Locate every Plasmodium ovale-infected red blood cell.
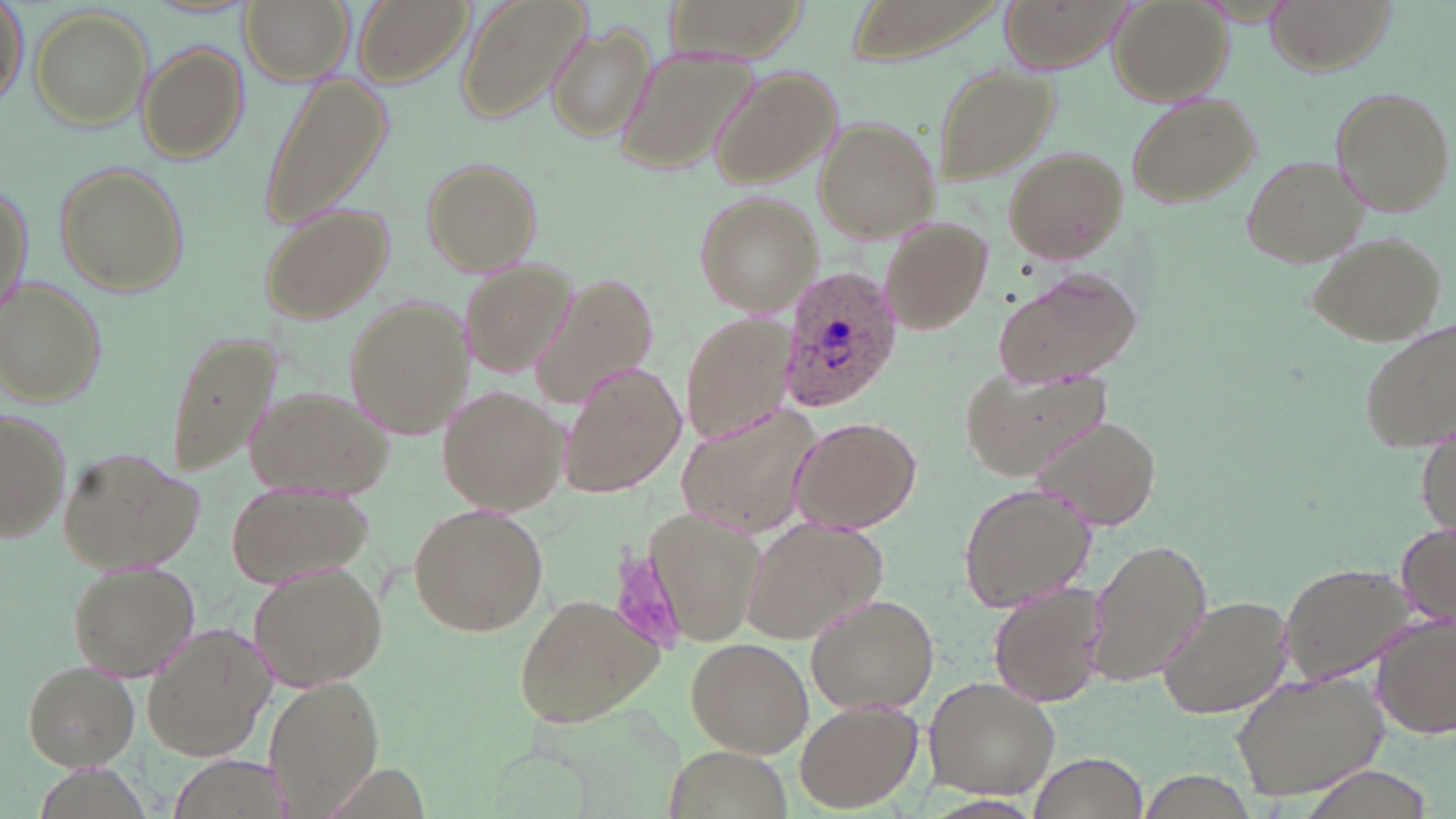

Approximate bounding boxes as [x1, y1, x2, y2] in pixels.
Plasmodium ovale-infected red blood cells: [779, 265, 902, 414].

Summary:
  - Uninfected red blood cell locations: [240, 0, 353, 84], [357, 0, 471, 84], [456, 0, 587, 119], [1001, 0, 1126, 69], [1108, 0, 1232, 106], [1263, 0, 1393, 72], [2, 1, 28, 108], [665, 3, 808, 69], [847, 3, 1000, 67], [30, 8, 153, 129], [548, 21, 655, 144], [137, 42, 247, 163], [615, 45, 757, 178], [928, 61, 1059, 185], [708, 66, 840, 191], [257, 72, 390, 228], [1328, 86, 1455, 217], [1124, 91, 1261, 209], [813, 114, 942, 244], [1003, 146, 1128, 262], [1240, 153, 1369, 266], [421, 157, 542, 278], [52, 162, 189, 300], [1, 175, 34, 315], [692, 190, 819, 316], [258, 204, 396, 326], [878, 216, 994, 335], [1308, 230, 1448, 344], [459, 258, 579, 377], [993, 266, 1143, 389], [534, 272, 660, 410], [0, 277, 108, 408], [343, 300, 474, 438], [682, 313, 793, 444], [1357, 320, 1454, 453], [163, 329, 282, 482], [560, 363, 684, 499], [959, 363, 1109, 484], [246, 384, 388, 493], [437, 387, 566, 515], [677, 398, 820, 537], [0, 406, 72, 548], [1032, 414, 1164, 534], [789, 415, 920, 532], [1416, 428, 1454, 541], [58, 445, 202, 575], [958, 480, 1094, 615], [227, 481, 373, 586], [408, 502, 549, 637], [644, 509, 769, 649], [741, 516, 886, 645], [1394, 522, 1456, 629], [1088, 538, 1212, 689], [68, 560, 199, 679], [249, 560, 388, 692], [1280, 561, 1414, 685], [987, 580, 1106, 705], [512, 592, 665, 730], [805, 593, 940, 716], [1157, 593, 1294, 718], [1372, 614, 1455, 740], [141, 625, 273, 760], [684, 636, 813, 757], [19, 659, 141, 769], [1231, 669, 1389, 801], [262, 674, 385, 814], [923, 677, 1063, 800], [793, 701, 920, 811], [657, 743, 794, 819], [1027, 750, 1151, 819]
  - Slide-level diagnosis: Plasmodium ovale
  - Modality: optical microscopy
  - Stain: May-Grünwald-Giemsa
  - Field of view: single
  - Magnification: 1000x
  - Preparation: thin blood smear
  - Image size: 1456×819 pixels